State the blood parasite species.
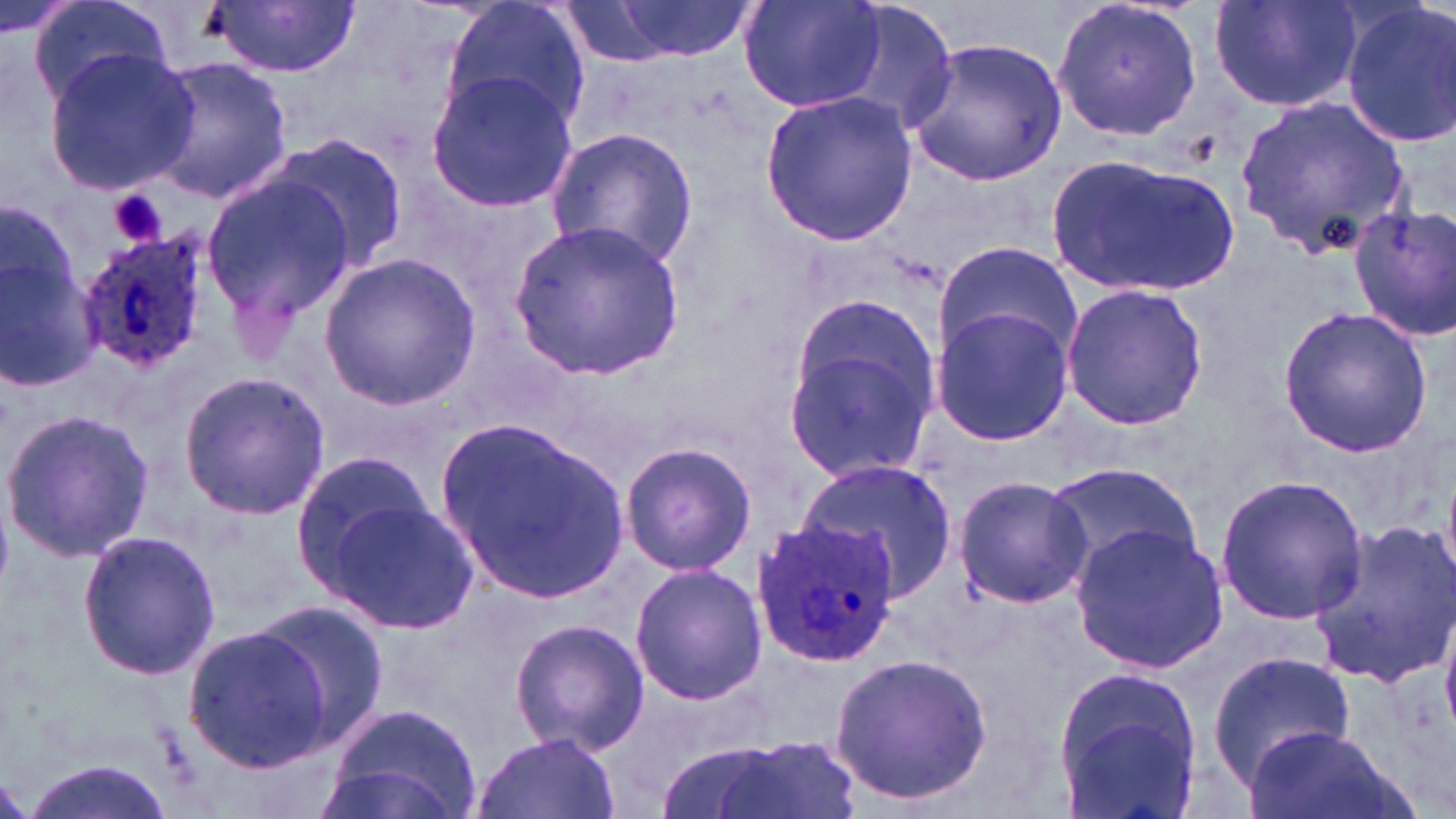
Plasmodium ovale.

{
  "platelet_locations": "approximate bounding boxes as named x1/y1/x2/y2 corners in pixels: (x1=108, y1=190, x2=166, y2=247)",
  "magnification": "1000x",
  "preparation": "thin blood film",
  "modality": "light microscopy",
  "field_of_view": "single",
  "plasmodium_ovale_infected_red_blood_cell_locations": "approximate bounding boxes as named x1/y1/x2/y2 corners in pixels: (x1=74, y1=236, x2=207, y2=375), (x1=752, y1=517, x2=902, y2=666)",
  "stain": "May-Grünwald-Giemsa",
  "image_size": "1456×819 pixels",
  "uninfected_red_blood_cell_locations": "approximate bounding boxes as named x1/y1/x2/y2 corners in pixels: (x1=440, y1=0, x2=592, y2=134), (x1=1052, y1=0, x2=1205, y2=144), (x1=1207, y1=0, x2=1365, y2=114), (x1=28, y1=1, x2=171, y2=103), (x1=208, y1=1, x2=360, y2=78), (x1=608, y1=1, x2=749, y2=61), (x1=1338, y1=1, x2=1456, y2=148), (x1=563, y1=2, x2=671, y2=65), (x1=740, y1=2, x2=885, y2=111), (x1=819, y1=2, x2=958, y2=138), (x1=905, y1=38, x2=1066, y2=185), (x1=43, y1=49, x2=199, y2=194), (x1=142, y1=57, x2=293, y2=203), (x1=427, y1=69, x2=576, y2=211), (x1=760, y1=89, x2=918, y2=247), (x1=1237, y1=97, x2=1412, y2=253), (x1=546, y1=126, x2=700, y2=268), (x1=276, y1=137, x2=408, y2=268), (x1=1049, y1=154, x2=1240, y2=297), (x1=202, y1=174, x2=359, y2=321), (x1=1348, y1=204, x2=1456, y2=340), (x1=511, y1=217, x2=686, y2=378), (x1=0, y1=222, x2=104, y2=397), (x1=936, y1=242, x2=1081, y2=366), (x1=319, y1=252, x2=481, y2=411), (x1=1060, y1=283, x2=1209, y2=432), (x1=1278, y1=306, x2=1433, y2=456), (x1=932, y1=307, x2=1074, y2=446), (x1=782, y1=316, x2=939, y2=481), (x1=177, y1=371, x2=332, y2=521), (x1=2, y1=406, x2=156, y2=562), (x1=439, y1=419, x2=630, y2=602), (x1=619, y1=441, x2=756, y2=577), (x1=287, y1=450, x2=436, y2=592), (x1=796, y1=459, x2=958, y2=603), (x1=1043, y1=463, x2=1204, y2=584), (x1=1214, y1=475, x2=1370, y2=624), (x1=954, y1=477, x2=1092, y2=609), (x1=327, y1=501, x2=481, y2=635), (x1=1305, y1=517, x2=1456, y2=689), (x1=1068, y1=524, x2=1226, y2=671), (x1=77, y1=529, x2=221, y2=680), (x1=630, y1=564, x2=768, y2=705), (x1=246, y1=602, x2=391, y2=750), (x1=508, y1=617, x2=650, y2=757), (x1=182, y1=621, x2=340, y2=774), (x1=1208, y1=652, x2=1355, y2=780), (x1=828, y1=653, x2=994, y2=806), (x1=1054, y1=668, x2=1203, y2=818), (x1=323, y1=702, x2=483, y2=819), (x1=1246, y1=725, x2=1395, y2=819), (x1=470, y1=732, x2=620, y2=819), (x1=708, y1=737, x2=859, y2=819), (x1=16, y1=752, x2=176, y2=819), (x1=313, y1=762, x2=462, y2=819)"
}